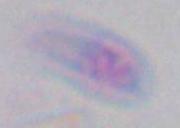

Summary:
  - Magnification: 1000x
  - Identification: Toxoplasma gondii
  - Modality: micrograph